Report the malaria status of this cell.
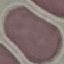

It is uninfected.

Summary:
  - Stain: Giemsa
  - Capture: smartphone through the microscope eyepiece
  - Image type: cell patch, automatically extracted from a larger field of view and resized to 64 × 64 pixels
  - Preparation: thin blood smear